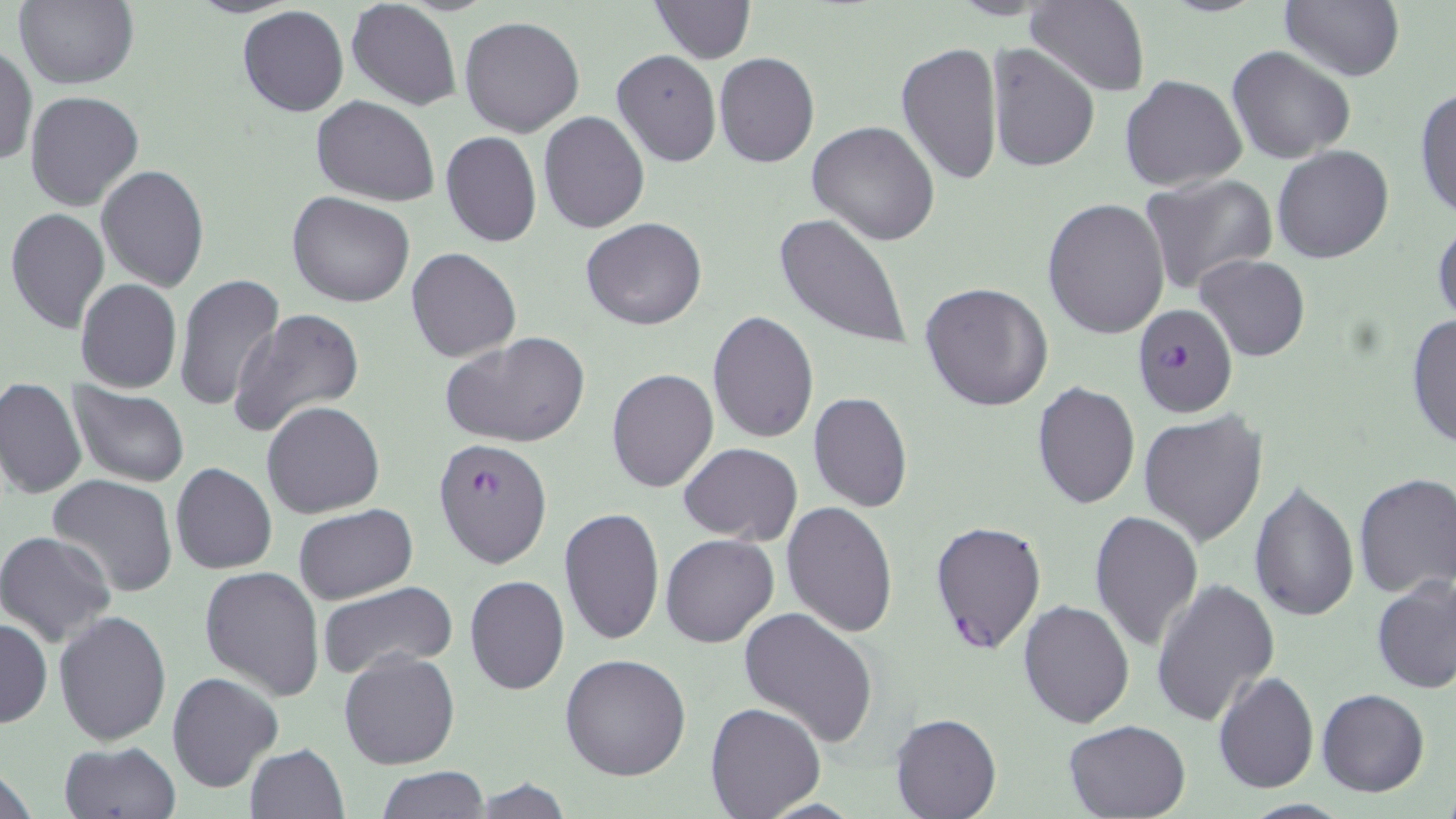
slide-level diagnosis = Plasmodium falciparum
stain = May-Grünwald-Giemsa
preparation = thin blood film
field of view = single
uninfected red blood cell locations = approximate bounding boxes as (x1,y1)-(x2,y2) corner pairs in pixels: (15,0)-(138,89), (347,0)-(462,111), (648,0)-(756,64), (1278,0)-(1403,82), (1024,1)-(1150,97), (237,6)-(348,116), (458,16)-(585,137), (896,41)-(1004,187), (986,42)-(1101,173), (0,45)-(36,168), (1227,46)-(1356,165), (613,49)-(721,167), (714,53)-(821,168), (1119,73)-(1247,193), (1413,83)-(1456,223), (24,89)-(145,211), (312,96)-(438,204), (539,111)-(649,232), (808,121)-(941,246), (440,131)-(541,247), (1271,145)-(1394,264), (96,166)-(209,292), (1139,174)-(1279,297), (287,192)-(416,308), (1041,198)-(1169,340), (5,207)-(112,333), (772,211)-(913,351), (1432,213)-(1455,330), (581,217)-(707,331), (407,248)-(522,363), (1193,253)-(1310,362), (173,274)-(285,412), (75,279)-(182,393), (920,281)-(1053,413), (229,304)-(370,440), (706,310)-(818,444), (1407,313)-(1455,452), (439,333)-(591,448), (606,369)-(719,493), (0,377)-(86,499), (1031,380)-(1140,510), (67,383)-(191,489), (809,392)-(912,511), (261,401)-(385,519), (1138,409)-(1269,547), (678,443)-(802,543), (171,463)-(277,575), (1352,472)-(1456,598), (48,475)-(179,597), (1249,480)-(1359,620), (781,502)-(898,637), (294,504)-(417,603), (558,507)-(666,648), (1088,510)-(1205,653), (0,531)-(117,647), (661,533)-(779,648), (199,565)-(325,700), (465,575)-(569,694), (1372,576)-(1455,695), (1150,579)-(1279,728), (317,582)-(458,679), (1018,599)-(1135,728), (738,605)-(879,746), (54,609)-(171,746), (0,618)-(50,728), (338,650)-(460,771), (559,652)-(691,780), (168,671)-(282,792), (1213,672)-(1319,792), (1318,689)-(1430,797), (704,701)-(827,819), (890,713)-(999,818), (1062,719)-(1191,819), (58,741)-(181,819), (244,744)-(350,819), (378,767)-(489,818), (464,779)-(577,817)
modality = optical microscopy
magnification = 1000x
Plasmodium falciparum-infected red blood cell locations = approximate bounding boxes as (x1,y1)-(x2,y2) corner pairs in pixels: (1134,303)-(1238,419), (433,436)-(553,569), (930,517)-(1047,656)
image size = 1456×819 pixels